Assess for malaria.
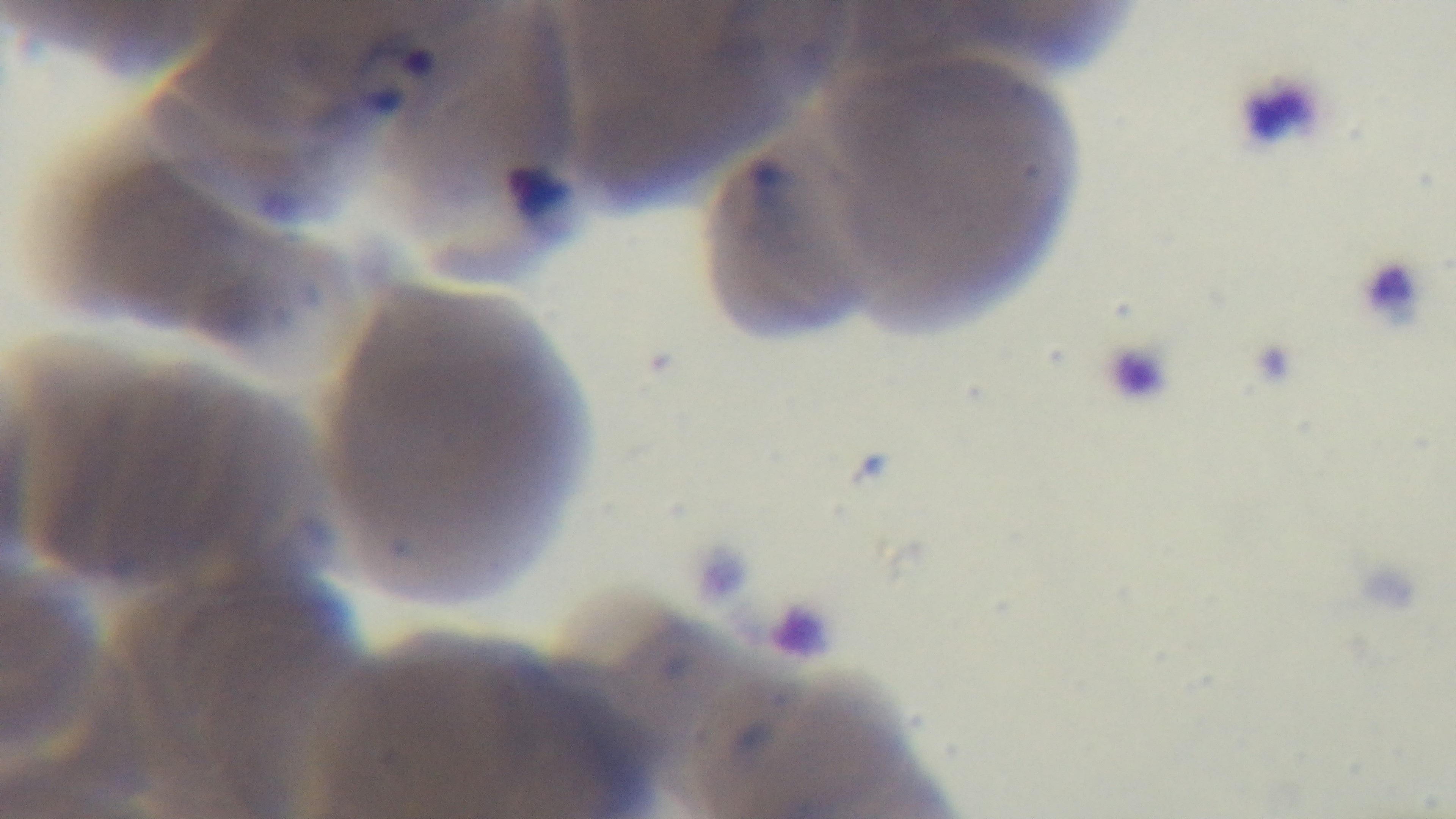

Infected.

Preparation: thin. Captured with a mounted 4K digital camera. One field from the slide. Giemsa-stained. Light microscopy. Oil-immersion objective, 100x.